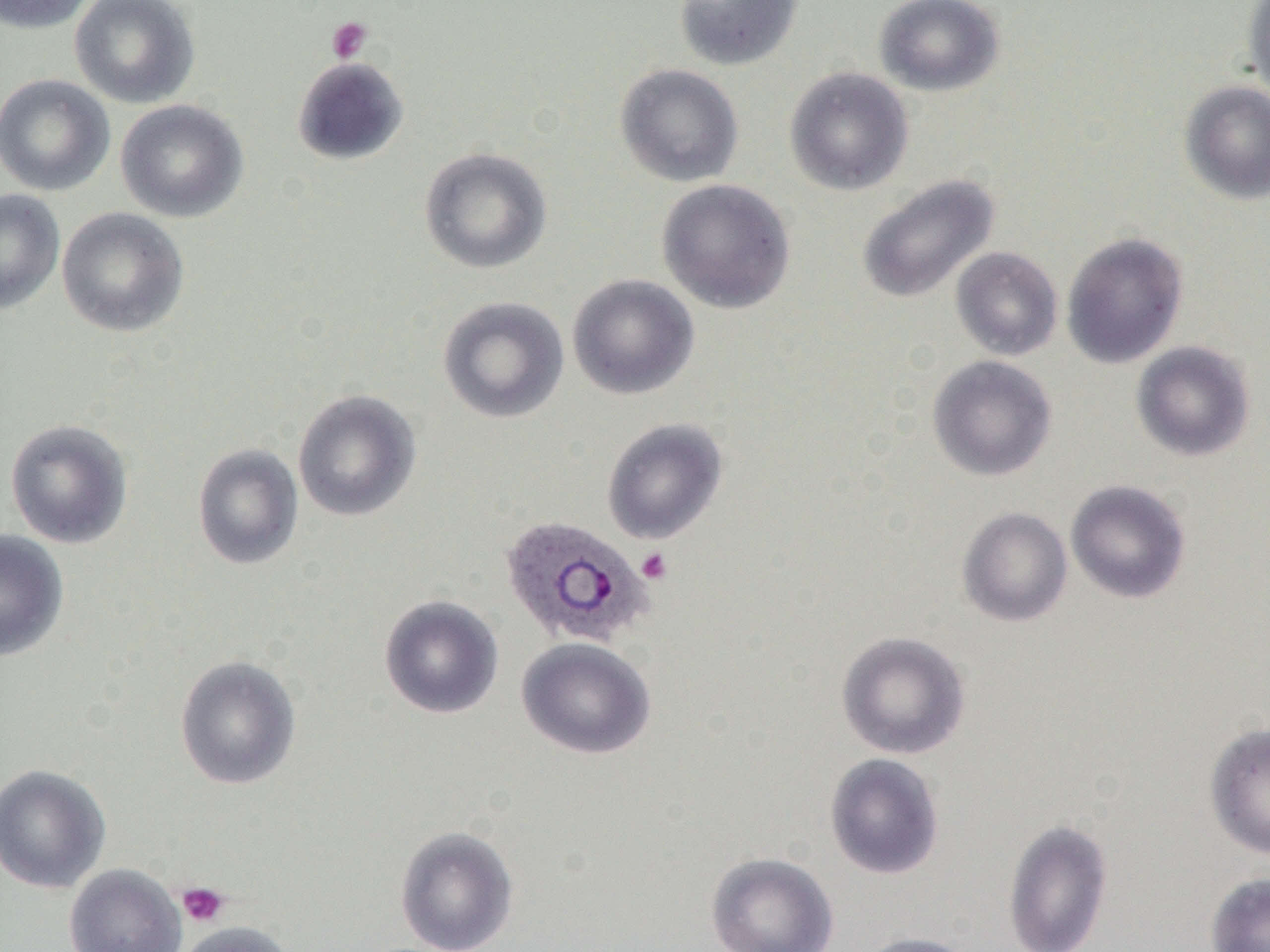
slide_level_diagnosis: Plasmodium ovale
uninfected_red_blood_cell_locations: 'approximate bounding boxes as named x1/y1/x2/y2 corners in pixels: (x1=0, y1=0, x2=98, y2=34), (x1=69, y1=0, x2=200, y2=109), (x1=674, y1=0, x2=803, y2=70), (x1=873, y1=0, x2=1005, y2=97), (x1=1241, y1=0, x2=1270, y2=106), (x1=292, y1=56, x2=409, y2=165), (x1=615, y1=63, x2=744, y2=188), (x1=783, y1=66, x2=914, y2=196), (x1=0, y1=73, x2=115, y2=197), (x1=1179, y1=80, x2=1270, y2=205), (x1=115, y1=99, x2=249, y2=222), (x1=419, y1=147, x2=552, y2=275), (x1=857, y1=173, x2=1000, y2=304), (x1=656, y1=179, x2=796, y2=314), (x1=0, y1=188, x2=65, y2=314), (x1=56, y1=207, x2=189, y2=337), (x1=1061, y1=232, x2=1188, y2=368), (x1=950, y1=246, x2=1063, y2=361), (x1=567, y1=274, x2=700, y2=400), (x1=437, y1=296, x2=569, y2=424), (x1=1131, y1=341, x2=1256, y2=461), (x1=927, y1=355, x2=1057, y2=481), (x1=292, y1=390, x2=422, y2=522), (x1=602, y1=418, x2=728, y2=544), (x1=4, y1=419, x2=133, y2=549), (x1=192, y1=443, x2=303, y2=570), (x1=1065, y1=480, x2=1191, y2=603), (x1=957, y1=507, x2=1073, y2=627), (x1=0, y1=530, x2=68, y2=661), (x1=379, y1=595, x2=504, y2=719), (x1=836, y1=631, x2=971, y2=760), (x1=516, y1=637, x2=656, y2=760), (x1=175, y1=655, x2=302, y2=790), (x1=1204, y1=722, x2=1270, y2=860), (x1=824, y1=753, x2=945, y2=880), (x1=0, y1=763, x2=110, y2=894), (x1=1002, y1=818, x2=1113, y2=952), (x1=394, y1=825, x2=519, y2=952), (x1=705, y1=851, x2=839, y2=952), (x1=63, y1=863, x2=186, y2=952), (x1=1206, y1=873, x2=1270, y2=952), (x1=176, y1=921, x2=296, y2=952), (x1=856, y1=932, x2=980, y2=952)'
modality: light microscopy
magnification: 1000x
preparation: thin blood film
plasmodium_ovale_infected_red_blood_cell_locations: 'approximate bounding boxes as named x1/y1/x2/y2 corners in pixels: (x1=499, y1=515, x2=654, y2=649)'
platelet_locations: 'approximate bounding boxes as named x1/y1/x2/y2 corners in pixels: (x1=326, y1=16, x2=373, y2=63), (x1=636, y1=547, x2=673, y2=584), (x1=177, y1=882, x2=230, y2=927)'
image_size: 1270×952 pixels
field_of_view: one of a larger specimen